Outline every leukocyte.
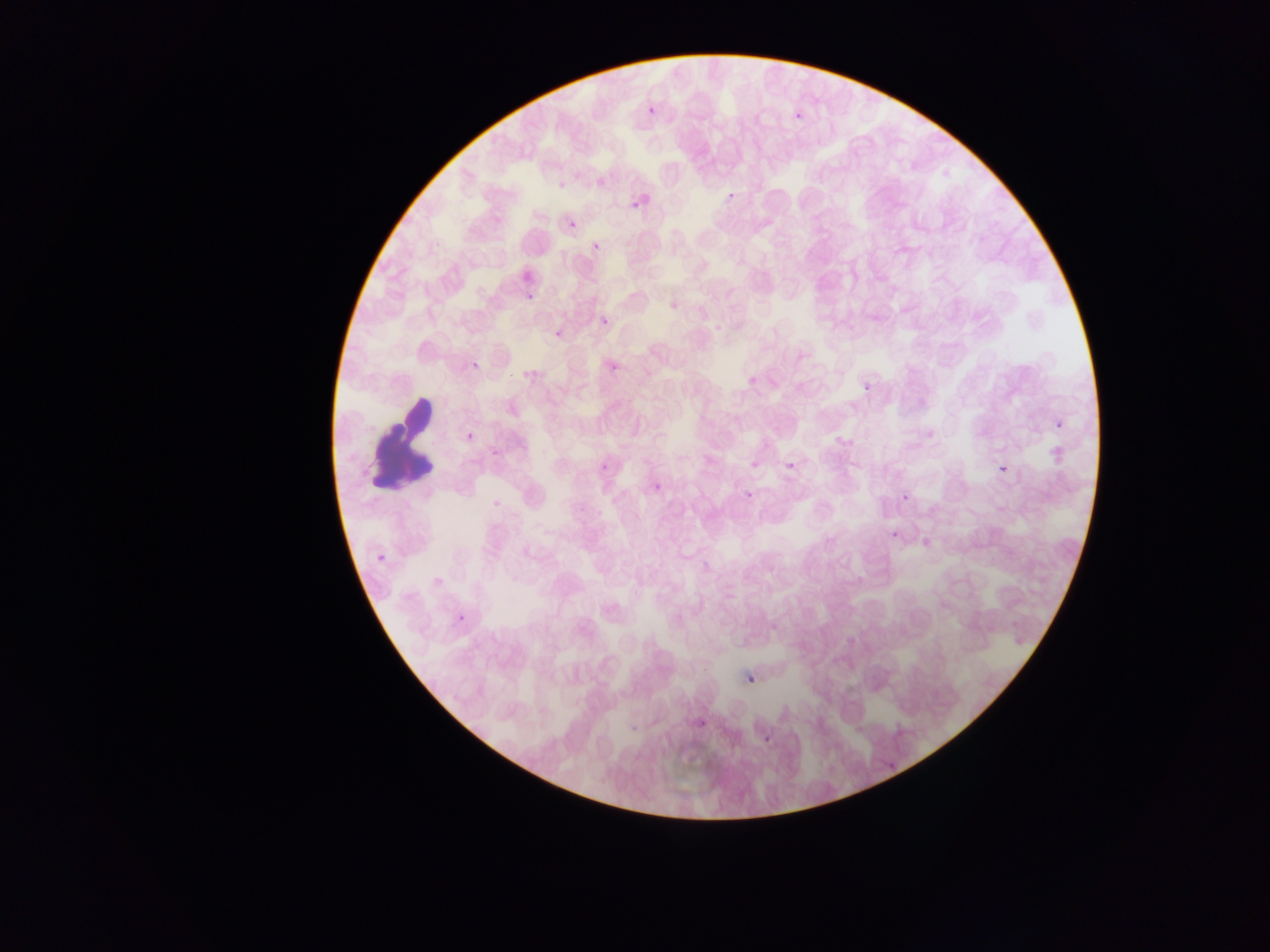
Approximate bounding boxes as {left, top, right, bottom} in pixels.
Leukocytes: {347, 357, 468, 507}.

field of view = single
country = Ghana
preparation = thin blood smear
Plasmodium parasite locations = approximate bounding boxes as {left, top, right, bottom} in pixels: {643, 96, 660, 115}, {790, 106, 808, 122}, {628, 193, 642, 206}, {726, 193, 734, 202}, {568, 221, 577, 230}, {590, 231, 607, 257}, {518, 284, 542, 305}, {595, 316, 612, 328}, {549, 320, 568, 344}, {608, 356, 627, 375}, {473, 359, 482, 375}, {740, 372, 758, 383}, {860, 372, 876, 394}, {1051, 411, 1068, 438}, {465, 426, 481, 452}, {990, 450, 1014, 480}, {596, 451, 615, 475}, {783, 456, 797, 470}, {741, 477, 753, 509}, {897, 480, 914, 496}, {653, 483, 662, 493}, {885, 520, 906, 542}, {372, 555, 389, 569}, {454, 609, 466, 621}, {747, 675, 756, 684}, {700, 705, 712, 728}, {760, 737, 770, 748}
capture = mobile-phone photograph through a microscope
image size = 1270×952 pixels